Locate and identify every blood parasite.
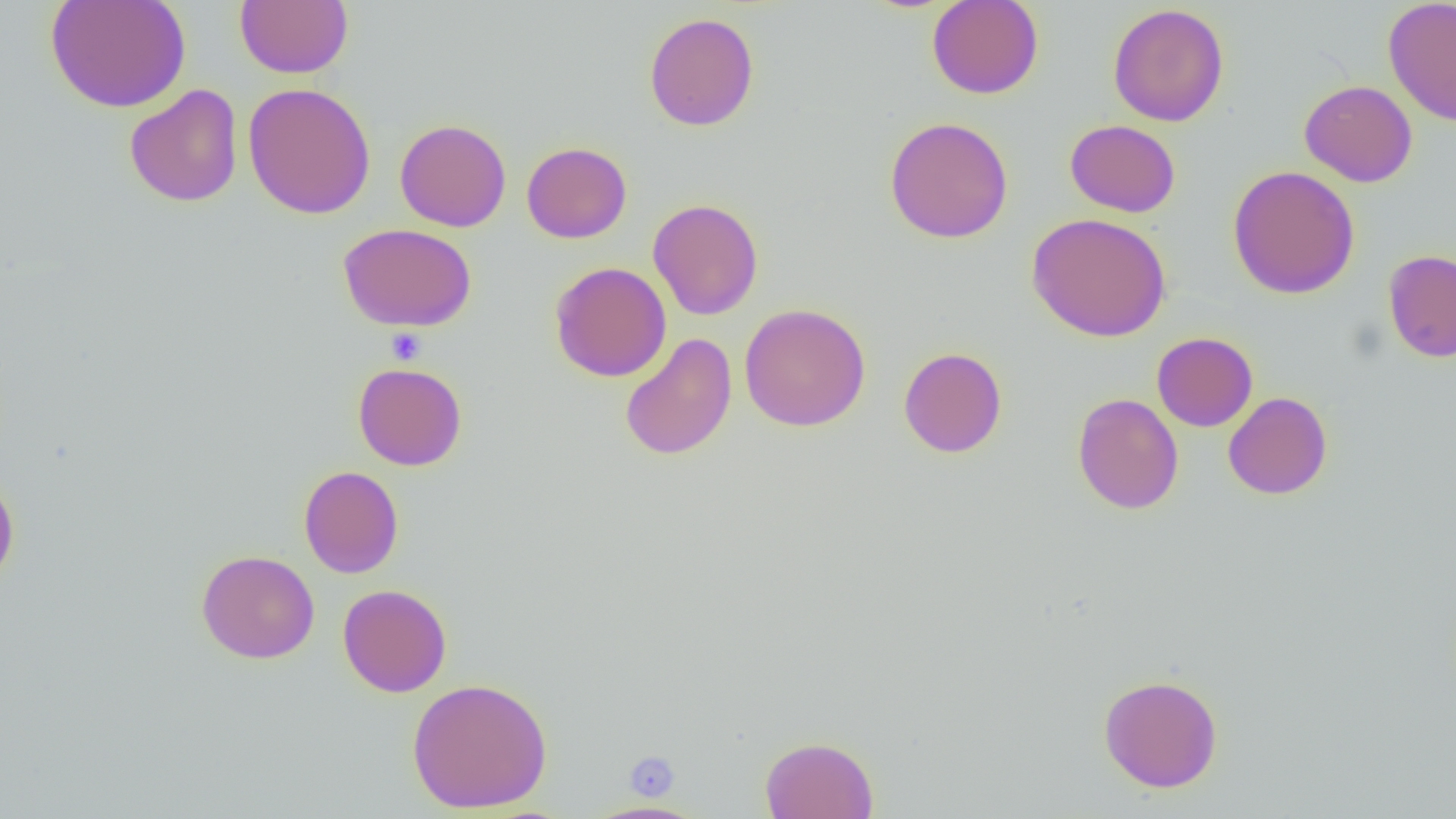
No blood parasites observed.

Summary:
  - Coordinate format: approximate bounding boxes as (x1,y1)-(x2,y2) corner pairs in pixels
  - Uninfected red blood cell locations: (46,0)-(191,112), (926,0)-(1044,99), (1383,0)-(1456,126), (235,1)-(354,78), (1107,4)-(1229,126), (644,12)-(760,132), (1299,80)-(1418,187), (242,82)-(376,219), (124,84)-(243,207), (884,116)-(1014,244), (394,118)-(511,232), (1065,119)-(1181,217), (521,141)-(631,243), (1228,165)-(1360,299), (648,198)-(764,320), (1027,212)-(1171,342), (338,223)-(477,331), (1383,249)-(1456,363), (549,261)-(671,382), (739,303)-(871,432), (1152,332)-(1258,431), (620,333)-(737,461), (898,347)-(1007,458), (353,363)-(467,471), (1223,392)-(1332,500), (1072,393)-(1184,514), (298,465)-(404,578), (0,471)-(20,590), (196,549)-(320,664), (338,583)-(452,697), (1098,674)-(1223,792), (407,677)-(553,813), (760,735)-(879,818), (581,800)-(709,818)
  - Platelet locations: (386,327)-(427,366), (623,751)-(679,800)
  - Slide-level diagnosis: negative for blood parasites
  - Modality: light microscopy
  - Preparation: thin blood film
  - Magnification: 1000x
  - Field of view: one of a larger specimen
  - Image size: 1456×819 pixels